Assess this cell for malaria.
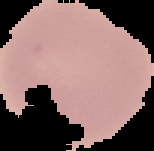

Uninfected.

From a thin blood film. Segmented cell region on a black background. Image is 154×151 pixels.